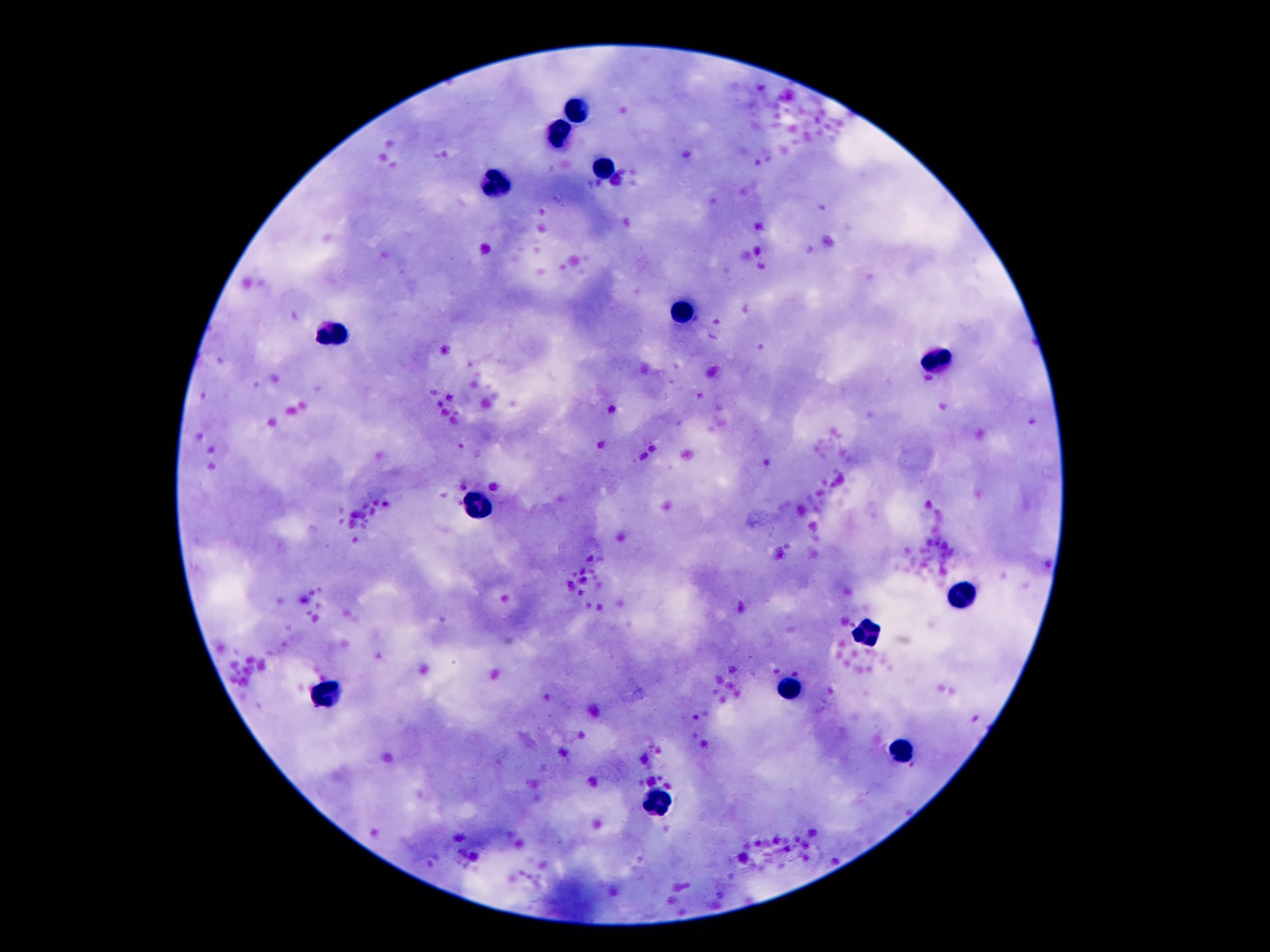

stain = Giemsa
leukocyte locations = approximate centers as (x, y) in pixels: (575, 108), (559, 131), (604, 165), (493, 187), (681, 308), (334, 333), (931, 362), (477, 509), (965, 592), (863, 631), (790, 685), (329, 689), (904, 744), (661, 801)
image size = 1270×952 pixels
magnification = 100x
preparation = thick peripheral-blood smear
patient malaria status = uninfected
field of view = single
capture = smartphone camera through the microscope eyepiece